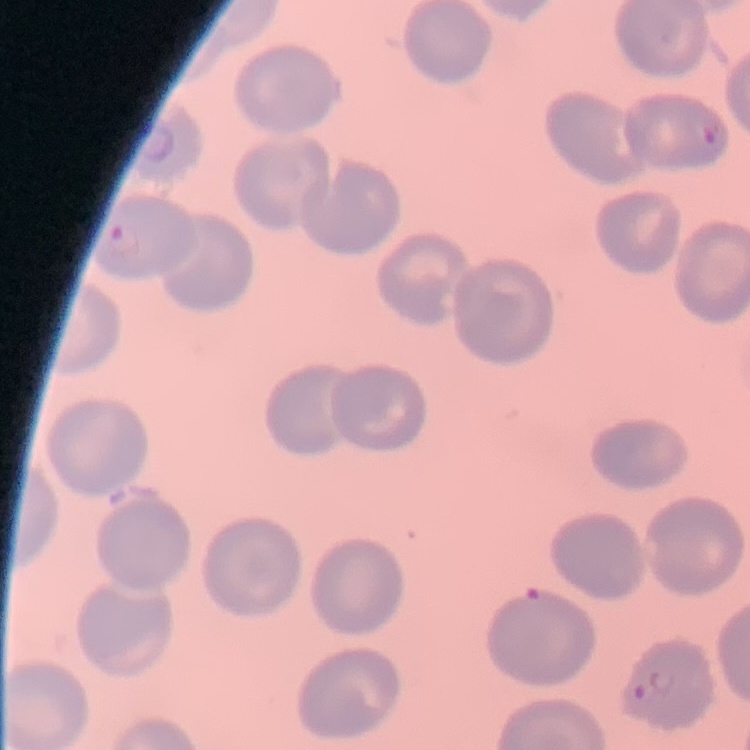
Summary:
  - Erythrocyte morphology: no rouleaux formation
  - Stain: Field's or Giemsa
  - Preparation: thin blood smear
  - Image type: square crop of a larger photomicrograph